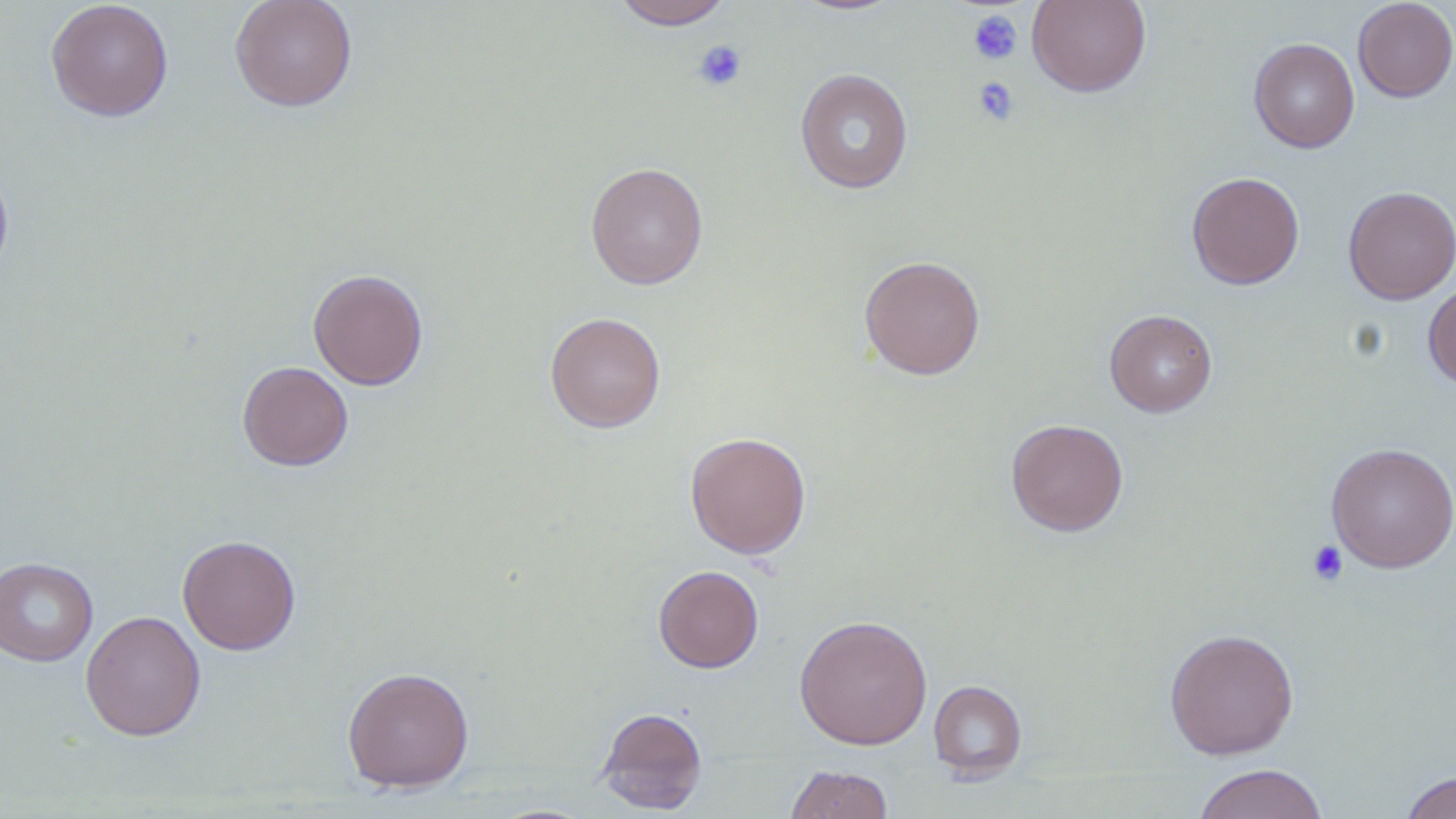

Summary:
  - Coordinate format: approximate bounding boxes as (x1,y1)-(x2,y2) corner pairs in pixels
  - Uninfected red blood cell locations: (45,0)-(174,122), (229,0)-(358,112), (613,0)-(732,30), (789,0)-(907,15), (1027,0)-(1151,97), (1353,0)-(1456,102), (1249,37)-(1359,153), (795,68)-(913,194), (0,160)-(14,286), (585,161)-(708,290), (1186,171)-(1305,289), (1343,186)-(1456,305), (858,254)-(986,380), (308,268)-(429,390), (1423,279)-(1456,389), (1104,309)-(1217,417), (545,311)-(666,433), (237,360)-(353,471), (1006,418)-(1128,536), (684,431)-(812,559), (1326,442)-(1456,573), (177,534)-(301,655), (0,557)-(98,666), (653,565)-(764,673), (80,610)-(206,741), (794,614)-(933,750), (1164,627)-(1299,760), (341,665)-(475,793), (928,680)-(1027,780), (596,706)-(708,814), (1192,763)-(1328,819), (786,765)-(892,819), (1400,770)-(1456,819)
  - Platelet locations: (969,10)-(1022,65), (693,40)-(747,92), (972,77)-(1019,126), (1307,540)-(1349,586)
  - Slide-level diagnosis: no evidence of blood parasites
  - Magnification: 1000x
  - Preparation: thin blood film
  - Image size: 1456×819 pixels
  - Stain: May-Grünwald-Giemsa
  - Field of view: one of a larger specimen
  - Modality: light microscopy